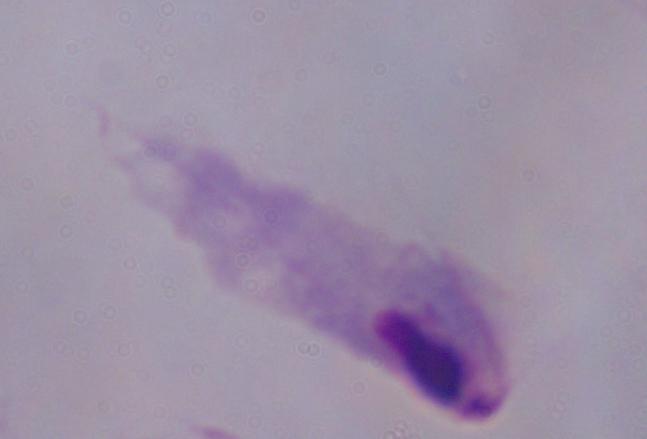
Photomicrograph. A trichomonad is seen. Captured at 1000x magnification.